Locate every malaria parasite.
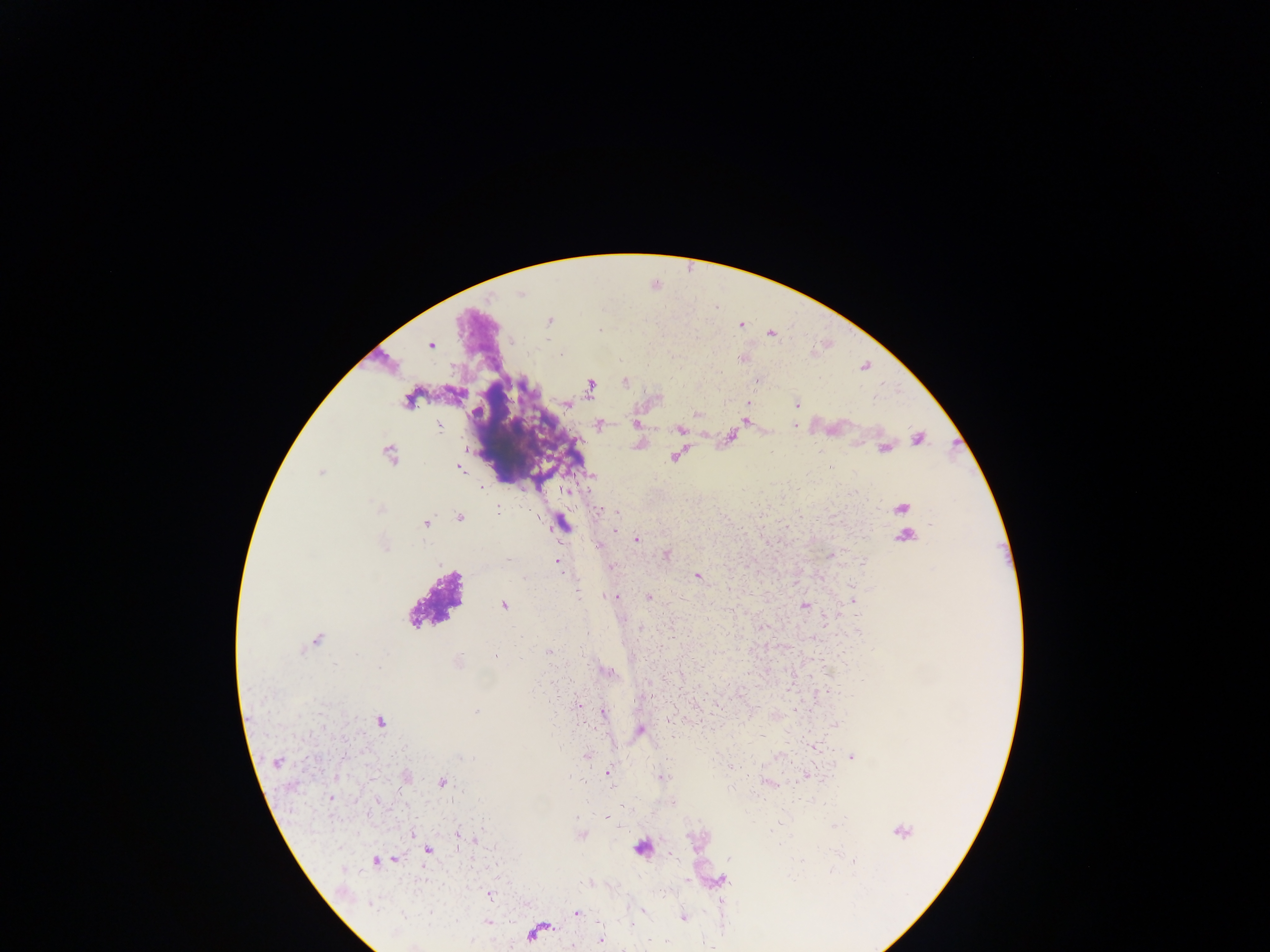
Approximate centers as x y in pixels.
Malaria parasites: 520 294; 550 321; 742 325; 600 330; 772 334; 430 344; 560 354; 625 382; 757 382; 591 386; 408 400; 748 403; 567 404; 796 405; 745 421; 635 424; 598 425; 795 425; 439 426; 679 428; 918 439; 884 449; 389 455; 674 457; 829 467; 460 468; 320 474; 591 476; 565 490; 499 507; 380 508; 902 508; 599 511; 616 513; 460 517; 724 519; 426 523; 562 524; 932 524; 788 526; 615 529; 906 536; 636 539; 598 545; 385 546; 667 555; 829 556; 508 561; 558 561; 863 561; 610 566; 697 576; 523 578; 616 596; 649 597; 852 600; 710 604; 504 606; 805 606; 588 633; 316 640; 514 644; 548 653; 495 657; 459 661; 379 667; 701 668; 608 672; 532 690; 578 705; 603 711; 476 712; 379 721; 836 724; 640 730; 673 736; 814 746; 587 756; 460 757; 852 758; 713 759; 276 763; 608 772; 406 776; 568 777; 661 777; 442 782; 584 782; 768 782; 614 788; 331 797; 577 817; 482 818; 607 818; 779 823; 834 826; 902 831; 413 834; 456 834; 474 841; 428 850; 729 859; 396 860; 375 862; 855 862; 832 870; 687 880; 491 895; 723 902; 372 904; 643 911; 430 913; 577 913; 403 916; 684 917; 489 922; 632 926; 600 940; 664 941.

image size = 1270×952 pixels
capture = mobile-phone photograph through a microscope
country = Ghana
field of view = single
preparation = thick blood smear